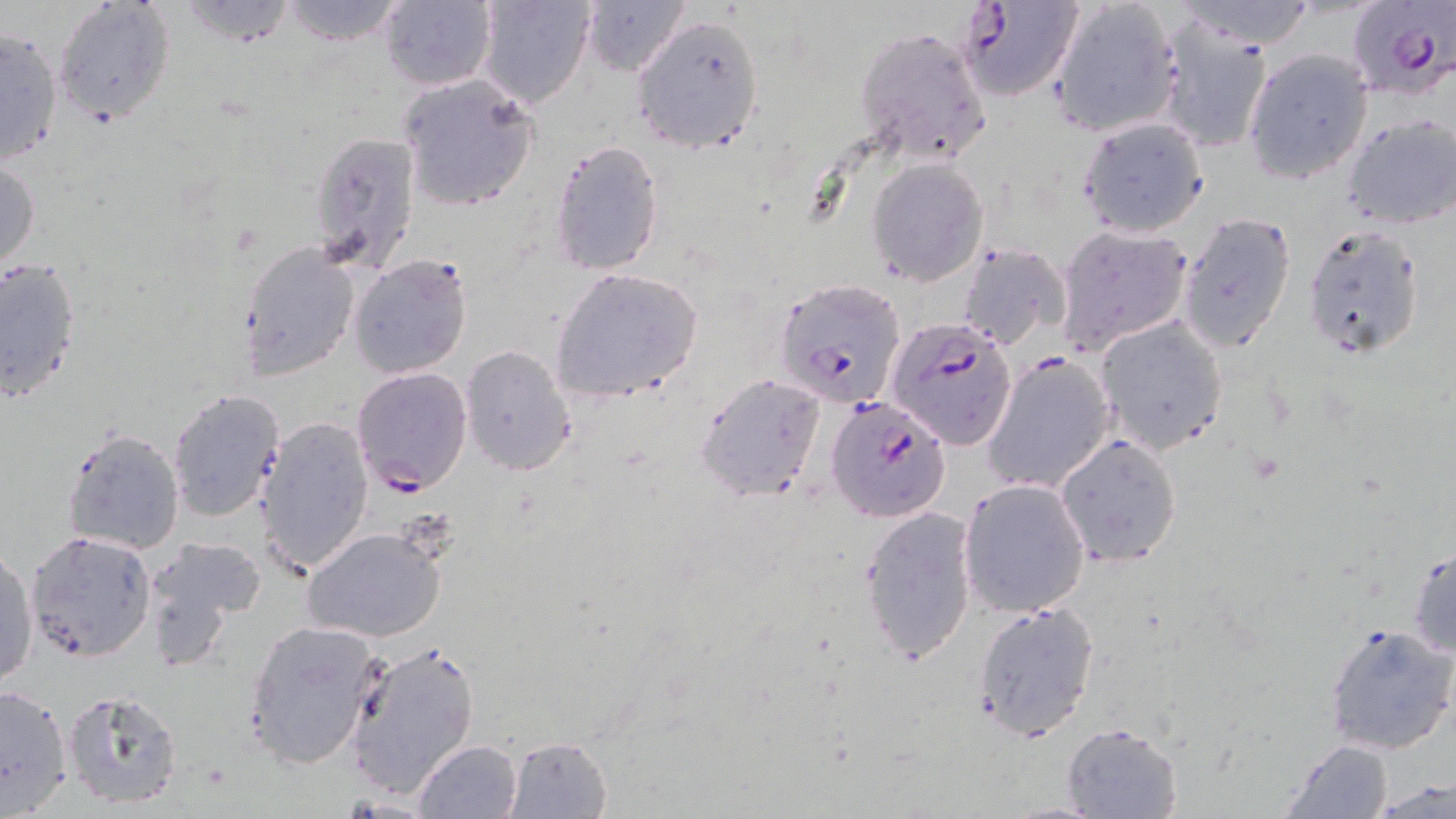

Summary:
  - Coordinate format: approximate bounding boxes as [x1, y1, x2, y2] in pixels
  - Plasmodium falciparum-infected red blood cell locations: [955, 0, 1084, 102], [1344, 0, 1456, 103], [777, 278, 907, 406], [886, 318, 1018, 450], [982, 351, 1117, 494], [351, 368, 472, 496], [825, 396, 950, 521]
  - Uninfected red blood cell locations: [170, 0, 299, 46], [273, 0, 411, 45], [379, 0, 498, 91], [475, 0, 596, 109], [580, 0, 690, 78], [1049, 0, 1180, 136], [1174, 0, 1318, 51], [52, 1, 175, 127], [631, 14, 764, 153], [1156, 17, 1275, 154], [0, 23, 65, 168], [853, 24, 993, 168], [1241, 48, 1372, 184], [396, 74, 539, 211], [1343, 114, 1456, 230], [1077, 116, 1208, 238], [308, 129, 422, 275], [548, 139, 666, 275], [0, 157, 41, 274], [867, 158, 991, 286], [1177, 210, 1298, 354], [1302, 222, 1427, 359], [1054, 225, 1192, 356], [239, 240, 360, 377], [955, 244, 1070, 351], [348, 254, 472, 378], [0, 256, 83, 404], [550, 268, 703, 402], [1093, 315, 1228, 455], [460, 345, 576, 477], [694, 372, 826, 502], [168, 389, 284, 521], [255, 416, 373, 575], [62, 428, 186, 555], [1054, 434, 1183, 566], [959, 477, 1091, 617], [859, 505, 979, 664], [302, 527, 448, 643], [25, 529, 157, 663], [144, 536, 265, 665], [1408, 544, 1455, 659], [1, 548, 37, 688], [970, 601, 1102, 742], [243, 619, 384, 770], [1323, 621, 1454, 756], [343, 637, 481, 797], [0, 683, 71, 815], [61, 688, 184, 810], [1060, 721, 1184, 817], [506, 734, 613, 817], [412, 739, 523, 818], [1280, 739, 1397, 817], [1371, 780, 1454, 817]
  - Slide-level diagnosis: Plasmodium falciparum
  - Image size: 1456×819 pixels
  - Modality: optical microscopy
  - Stain: May-Grünwald-Giemsa
  - Magnification: 1000x
  - Preparation: thin blood smear
  - Field of view: single